Assess the morphology of the red blood cells.
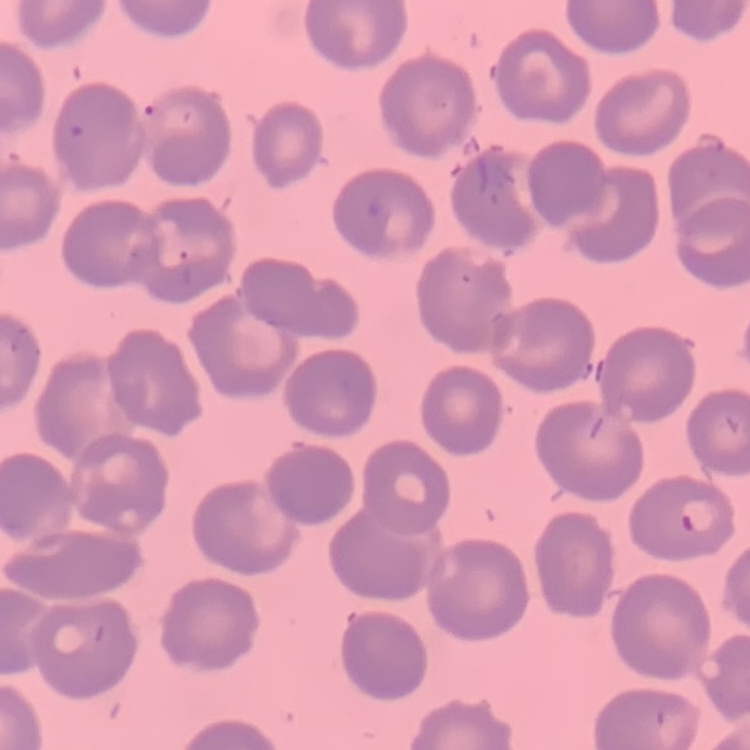
No rouleaux formation.

Field's or Giemsa stain. Thin peripheral smear. Square crop of a larger photomicrograph.